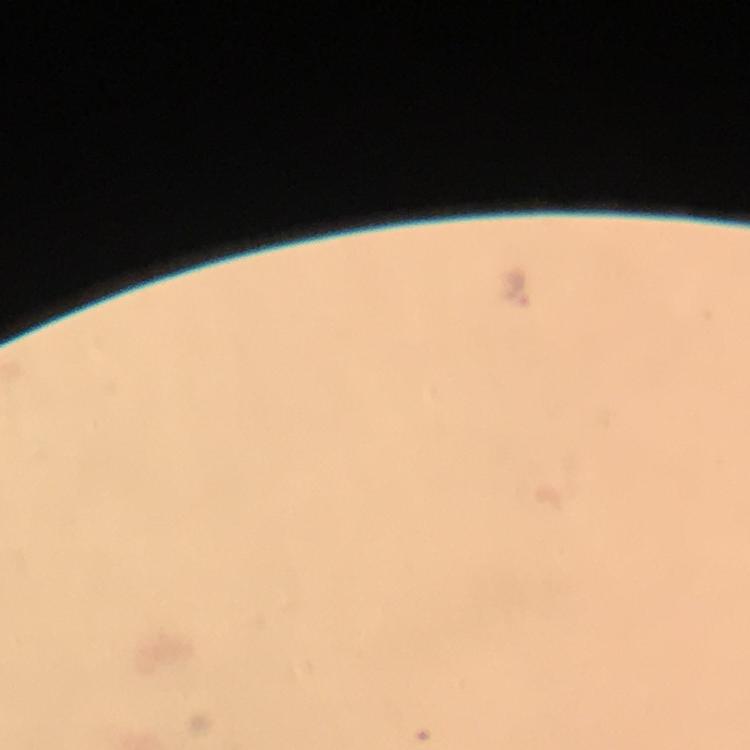

Approximate centers as {x, y} in pixels. Malaria parasite locations: {517, 285}. Smartphone photograph taken through a microscope. A crop from one field of view. Image is 750×750 pixels. From a malaria diagnostic workup. Thick blood smear. Immersion oil applied. Giemsa-stained preparation. At 100x magnification.